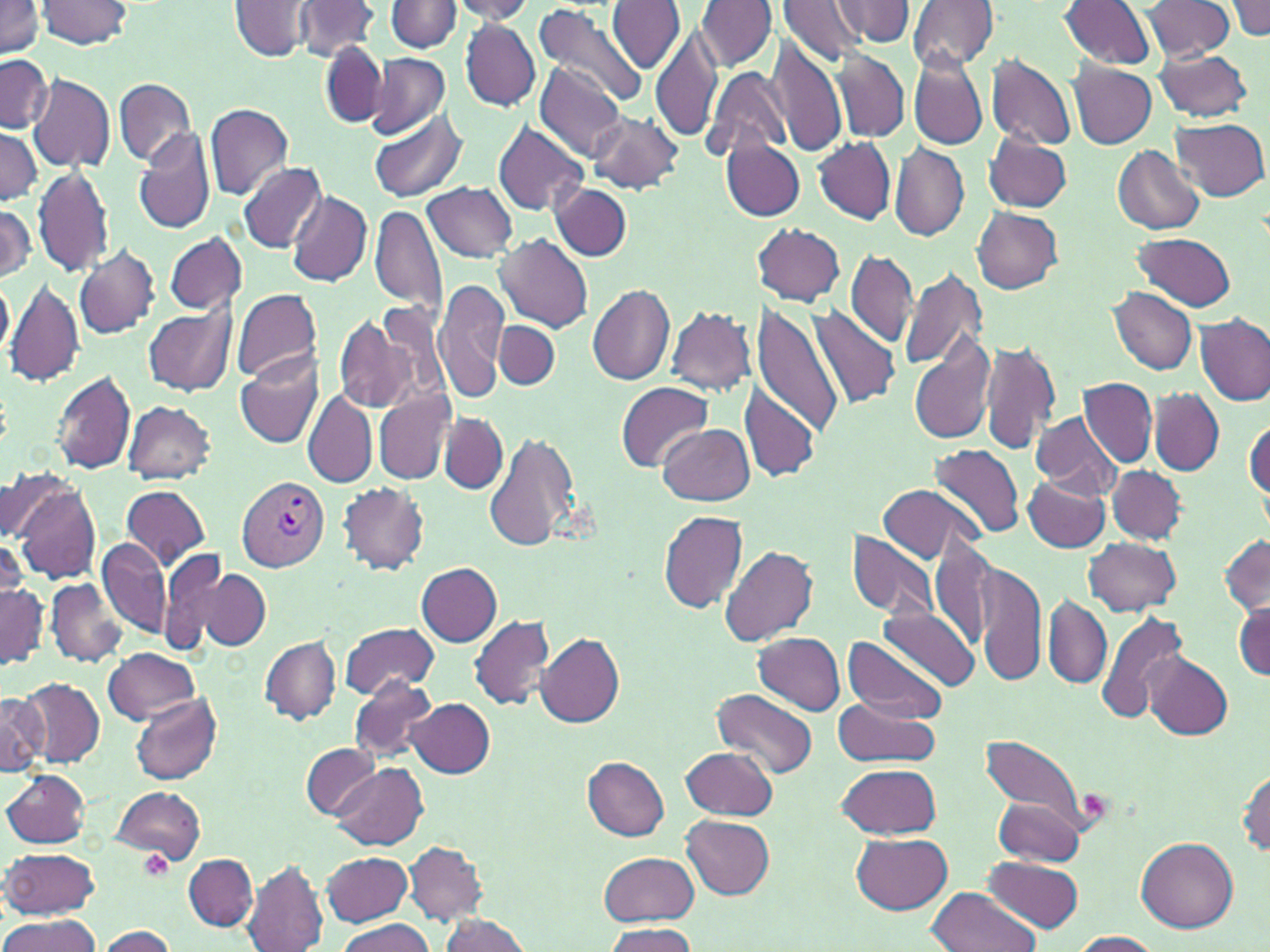
Summary:
  - Coordinate format: approximate bounding boxes as [x1, y1, x2, y2] in pixels
  - Uninfected red blood cell locations: [294, 0, 379, 61], [695, 0, 776, 70], [831, 0, 913, 47], [908, 0, 999, 72], [1227, 0, 1270, 41], [0, 1, 47, 58], [35, 1, 135, 50], [387, 1, 462, 52], [445, 1, 538, 24], [608, 1, 685, 75], [778, 1, 864, 66], [1060, 1, 1158, 69], [1142, 1, 1233, 61], [230, 2, 315, 61], [534, 2, 646, 109], [460, 20, 540, 111], [650, 26, 722, 143], [766, 36, 847, 159], [319, 42, 388, 127], [1154, 48, 1254, 121], [833, 49, 910, 144], [0, 53, 52, 134], [365, 53, 452, 139], [986, 54, 1076, 150], [909, 55, 987, 151], [535, 63, 625, 164], [1067, 63, 1156, 149], [703, 66, 791, 164], [26, 73, 116, 172], [114, 78, 196, 166], [204, 104, 293, 201], [369, 108, 469, 202], [587, 111, 685, 194], [1171, 118, 1268, 200], [491, 120, 589, 217], [0, 127, 41, 206], [135, 128, 215, 235], [983, 132, 1072, 214], [812, 137, 896, 223], [723, 139, 804, 222], [890, 142, 969, 243], [1112, 145, 1205, 237], [240, 162, 326, 252], [32, 165, 114, 279], [422, 182, 518, 263], [552, 185, 632, 260], [287, 190, 372, 287], [0, 203, 35, 282], [370, 204, 447, 317], [972, 207, 1064, 294], [754, 223, 846, 305], [1132, 231, 1236, 312], [165, 232, 247, 314], [496, 233, 594, 332], [74, 245, 161, 340], [845, 249, 918, 347], [900, 266, 987, 371], [0, 276, 14, 361], [6, 276, 85, 389], [434, 277, 508, 399], [587, 284, 675, 385], [1108, 286, 1196, 375], [231, 288, 322, 385], [365, 300, 446, 409], [750, 302, 845, 438], [144, 305, 236, 396], [665, 306, 756, 395], [807, 306, 902, 409], [334, 312, 417, 414], [1196, 313, 1270, 405], [495, 319, 558, 390], [910, 335, 995, 446], [980, 340, 1061, 456], [234, 353, 323, 450], [52, 370, 136, 476], [1079, 377, 1157, 467], [616, 382, 712, 471], [741, 384, 820, 483], [374, 389, 456, 484], [1149, 390, 1224, 475], [304, 391, 378, 487], [122, 400, 216, 482], [1032, 410, 1121, 497], [439, 412, 507, 495], [1245, 420, 1270, 500], [659, 425, 754, 505], [485, 429, 582, 554], [931, 444, 1023, 542], [1108, 465, 1185, 544], [4, 468, 80, 544], [1023, 475, 1111, 552], [10, 481, 101, 583], [338, 482, 430, 575], [121, 484, 211, 571], [877, 484, 980, 565], [658, 509, 749, 613], [846, 532, 939, 622], [0, 535, 29, 620], [1219, 535, 1270, 614], [928, 536, 998, 648], [1084, 537, 1181, 616], [96, 539, 169, 637], [720, 545, 818, 647], [162, 548, 232, 651], [975, 561, 1045, 685], [416, 563, 501, 645], [193, 568, 270, 652], [47, 580, 126, 667], [0, 582, 49, 666], [1043, 594, 1111, 689], [1233, 600, 1269, 680], [880, 603, 979, 693], [1094, 610, 1192, 726], [470, 615, 556, 709], [339, 622, 439, 701], [535, 630, 624, 727], [754, 632, 845, 715], [260, 635, 340, 724], [841, 635, 947, 723], [103, 647, 198, 723], [1142, 651, 1233, 739], [348, 676, 439, 763], [18, 678, 105, 766], [711, 689, 819, 780], [1, 692, 48, 776], [130, 693, 222, 785], [832, 696, 941, 767], [409, 698, 494, 777], [977, 728, 1102, 836], [302, 744, 379, 817], [680, 746, 777, 820], [582, 757, 669, 839], [330, 763, 427, 849], [835, 764, 942, 838], [1237, 767, 1269, 859], [2, 770, 89, 848], [109, 785, 206, 865], [993, 797, 1085, 867], [681, 816, 774, 898], [852, 833, 953, 915], [1136, 836, 1239, 933], [404, 841, 488, 925], [3, 845, 100, 919], [324, 852, 413, 927], [598, 852, 699, 926], [184, 854, 258, 931], [241, 857, 329, 952], [982, 857, 1084, 934], [325, 886, 426, 952], [925, 886, 1038, 952], [436, 913, 533, 951], [0, 915, 101, 952], [336, 919, 437, 952], [599, 922, 699, 951], [98, 926, 177, 951], [1069, 931, 1163, 951]
  - Plasmodium vivax-infected red blood cell locations: [238, 477, 330, 571]
  - Platelet locations: [138, 851, 172, 880]
  - Slide-level diagnosis: Plasmodium vivax
  - Modality: optical microscopy
  - Stain: May-Grünwald-Giemsa
  - Field of view: single
  - Magnification: 1000x
  - Preparation: thin blood film
  - Image size: 1270×952 pixels